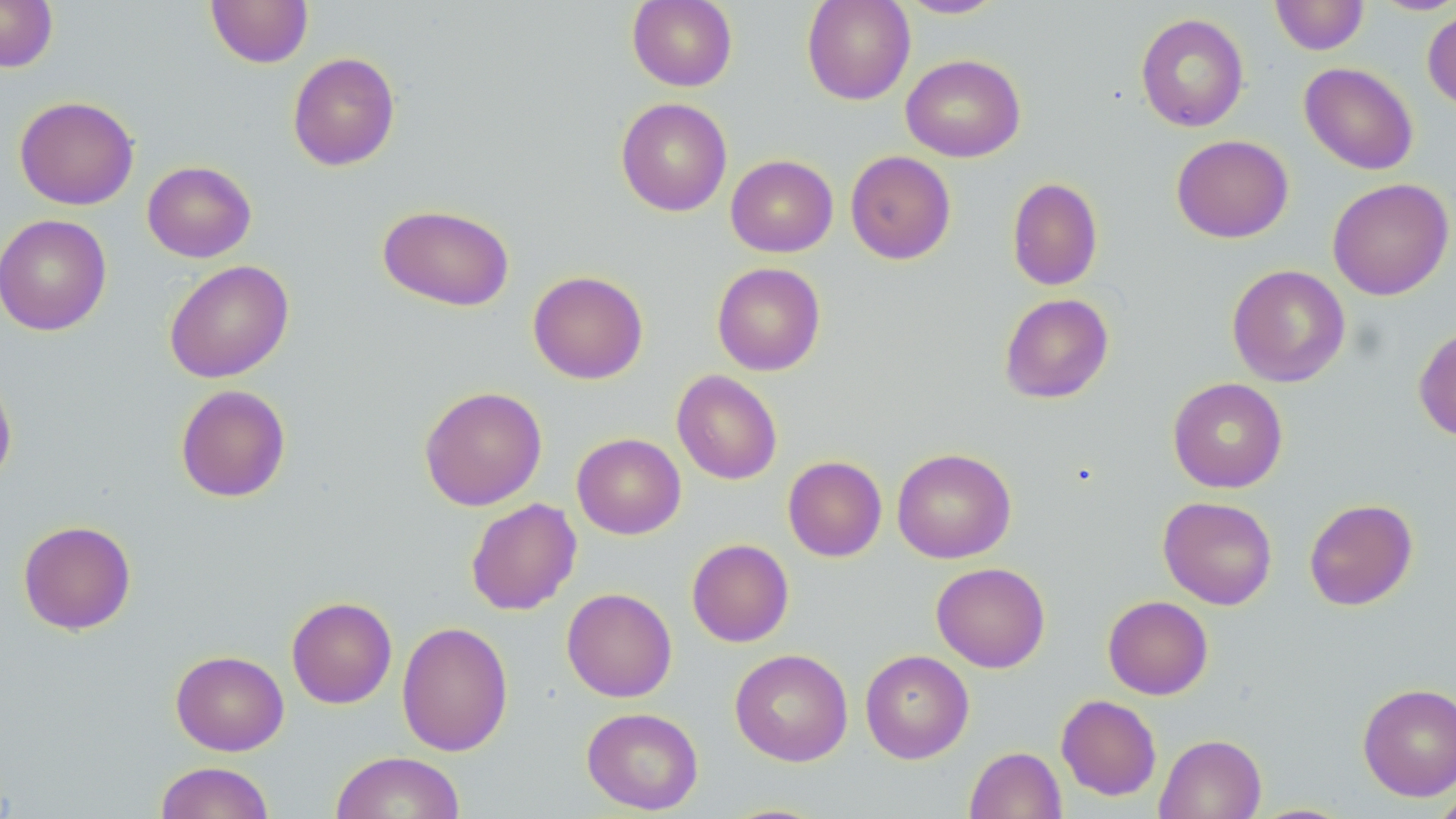

slide-level diagnosis = negative for blood parasites
modality = light microscopy
uninfected red blood cell locations = approximate bounding boxes as [x1, y1, x2, y2] in pixels: [0, 0, 58, 72], [206, 0, 313, 68], [627, 0, 738, 91], [801, 0, 916, 105], [896, 0, 1008, 19], [1270, 0, 1369, 55], [1369, 1, 1456, 16], [1422, 8, 1456, 110], [1135, 13, 1249, 133], [287, 51, 400, 171], [901, 54, 1025, 162], [1299, 62, 1418, 174], [14, 95, 139, 210], [616, 97, 732, 216], [1171, 134, 1293, 243], [845, 150, 956, 264], [725, 154, 838, 257], [142, 160, 256, 262], [1006, 177, 1103, 291], [1326, 177, 1454, 300], [378, 204, 515, 311], [0, 213, 112, 336], [164, 260, 294, 383], [711, 262, 826, 376], [1227, 264, 1350, 387], [528, 270, 648, 384], [999, 293, 1113, 404], [1414, 324, 1456, 442], [0, 369, 17, 487], [671, 370, 783, 484], [1168, 377, 1288, 493], [175, 384, 291, 502], [419, 386, 547, 510], [572, 433, 686, 539], [891, 447, 1016, 563], [783, 455, 886, 562], [1158, 496, 1277, 610], [465, 498, 582, 615], [1304, 498, 1418, 610], [18, 519, 136, 635], [686, 539, 794, 647], [931, 562, 1050, 672], [562, 587, 677, 702], [1102, 595, 1213, 699], [287, 596, 397, 708], [396, 621, 513, 756], [730, 648, 853, 766], [860, 649, 974, 764], [170, 650, 289, 756], [1357, 683, 1456, 801], [1056, 694, 1162, 800], [581, 707, 704, 814], [1155, 733, 1266, 819], [964, 746, 1066, 819], [331, 751, 466, 819], [154, 761, 274, 819], [1430, 788, 1456, 818]
field of view = one of a larger specimen
stain = May-Grünwald-Giemsa
magnification = 1000x
image size = 1456×819 pixels
preparation = thin blood film